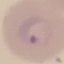

malaria status = parasitized
image type = automatically extracted cell patch, resized to 64 × 64 pixels
preparation = thin blood smear
stain = Giemsa
capture = smartphone camera at the microscope eyepiece